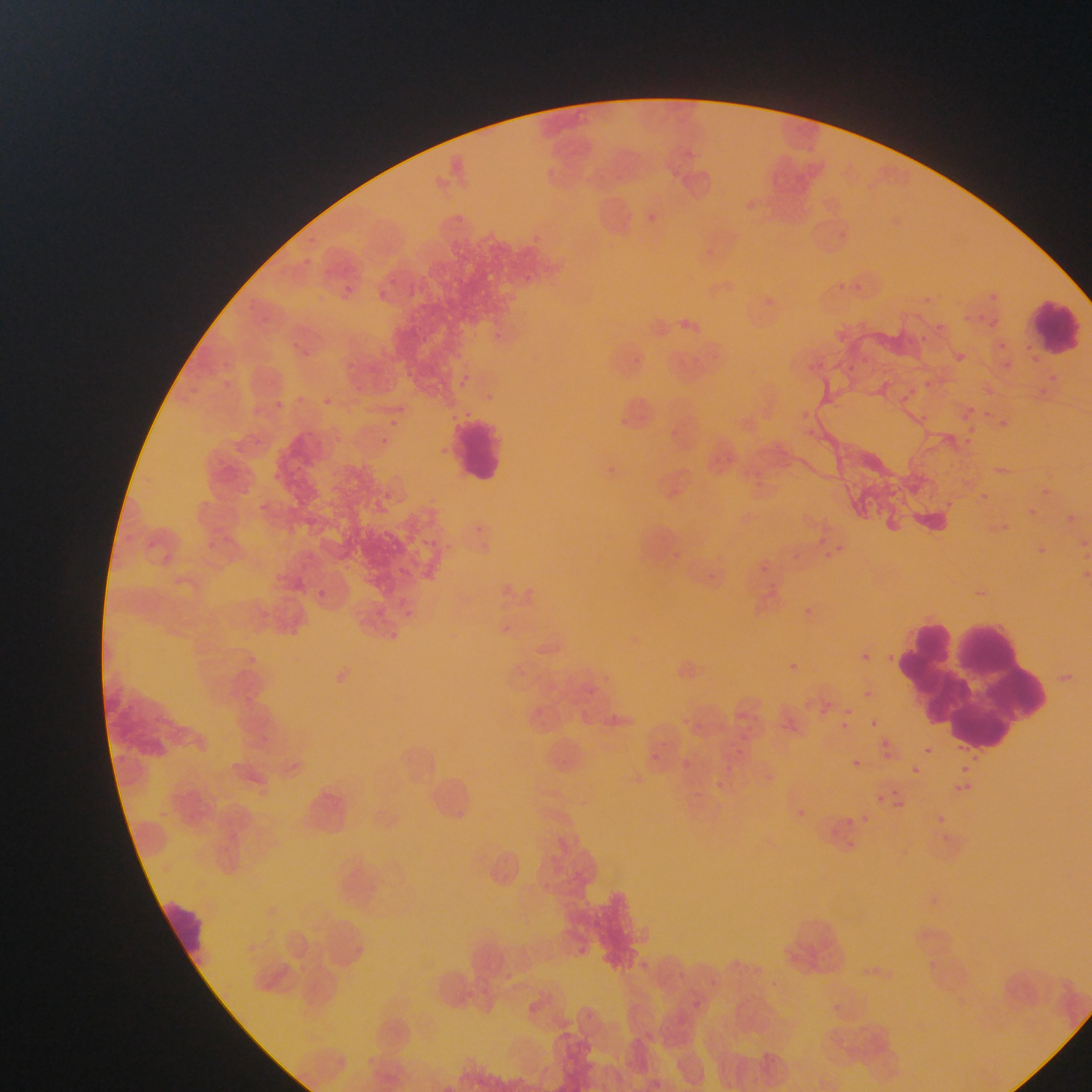

Approximate bounding boxes as {left, top, right, bottom} in pixels.
Summary:
  - Leukocyte locations: {1032, 296, 1092, 369}, {447, 418, 533, 493}, {909, 624, 1068, 747}, {164, 892, 212, 961}
  - Image size: 1092×1092 pixels
  - Country: Ghana
  - Field of view: single
  - Capture: mobile-phone photograph through a microscope
  - Preparation: thin blood film